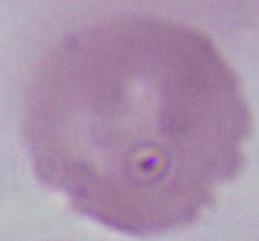
Summary:
  - Magnification: 1000x
  - Modality: photomicrograph
  - Identification: erythrocyte